Comment on the morphology of the erythrocytes.
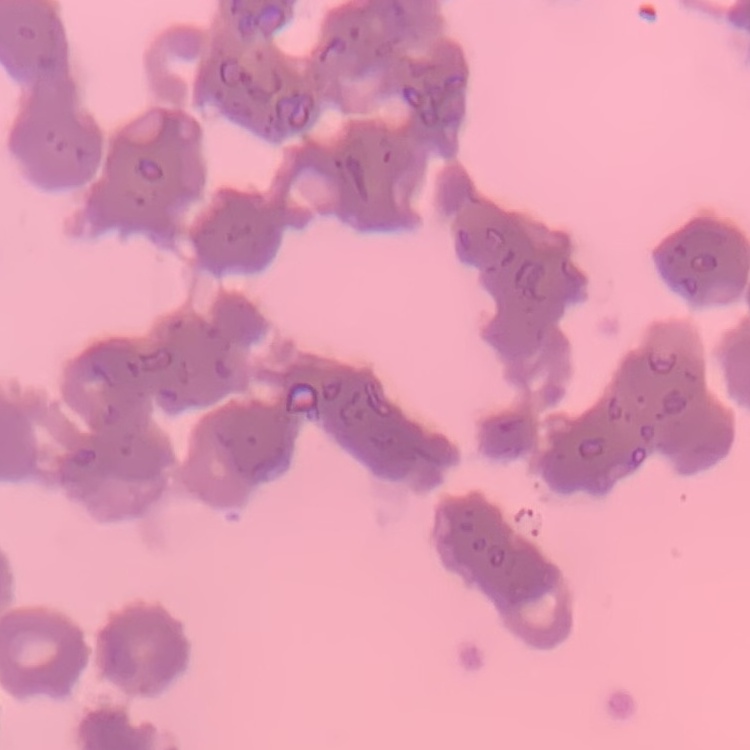

They show rouleaux formation.

stain: Field's or Giemsa
image_type: one tile cut from a larger photomicrograph
preparation: thin peripheral smear